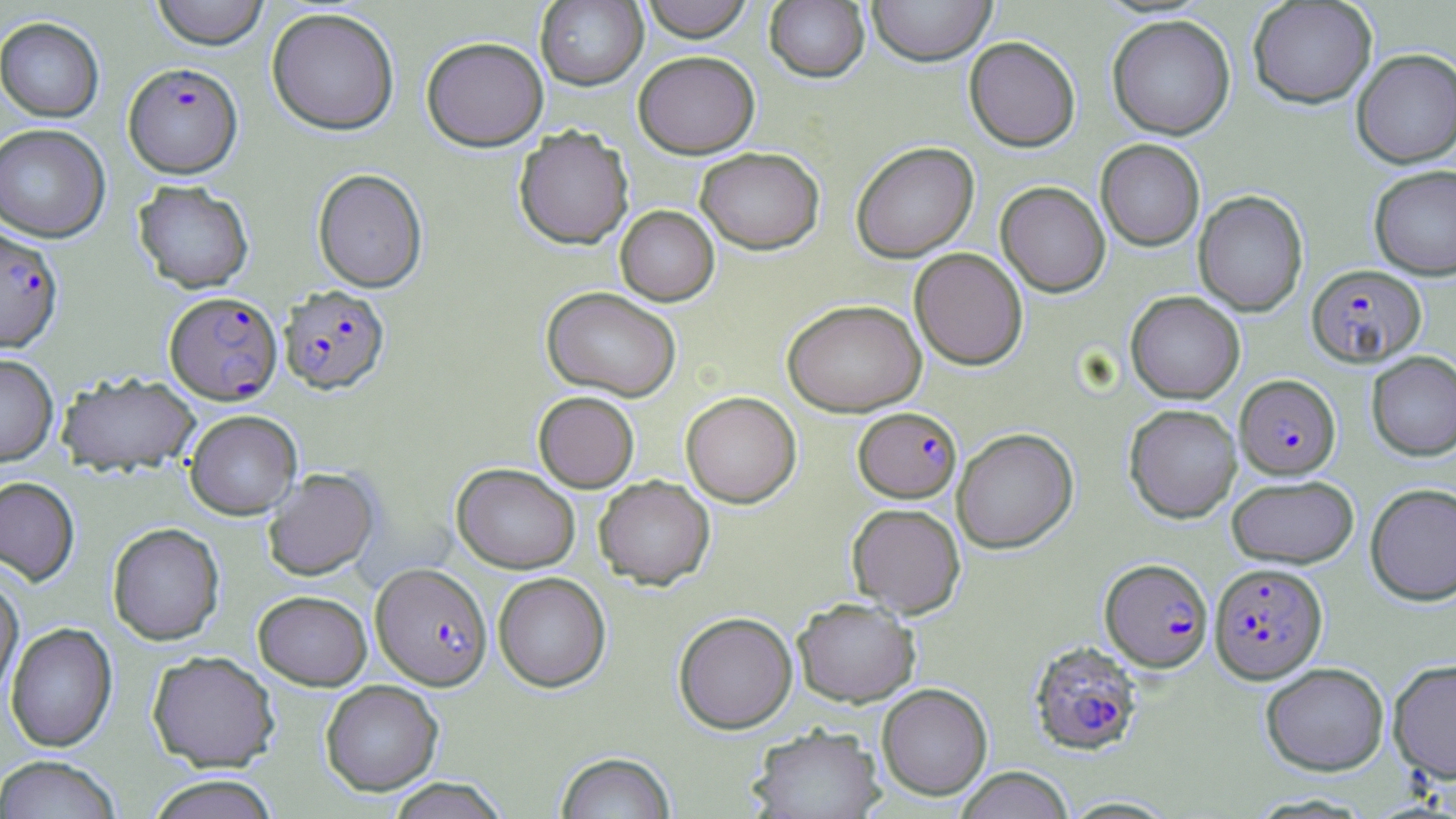

Approximate bounding boxes as (x1, y1, x2, y2) in pixels. Plasmodium falciparum-infected red blood cell locations: (123, 61, 243, 178), (0, 226, 64, 353), (1306, 264, 1426, 368), (279, 285, 390, 394), (165, 291, 282, 404), (1235, 374, 1340, 479), (854, 407, 961, 502), (1100, 558, 1213, 672), (370, 562, 492, 690), (1209, 562, 1328, 683), (1028, 640, 1144, 756). Uninfected red blood cell locations: (150, 0, 270, 49), (639, 0, 754, 41), (867, 0, 997, 66), (535, 1, 648, 90), (764, 1, 870, 83), (1247, 1, 1377, 108), (266, 6, 400, 135), (1107, 14, 1236, 140), (0, 16, 104, 122), (421, 36, 549, 151), (964, 36, 1081, 151), (1351, 48, 1456, 168), (634, 50, 760, 158), (0, 123, 111, 242), (514, 125, 633, 249), (1095, 139, 1205, 251), (851, 141, 979, 262), (695, 147, 824, 254), (1369, 165, 1456, 280), (312, 168, 428, 293), (133, 179, 255, 293), (996, 181, 1110, 296), (1193, 190, 1308, 317), (615, 205, 719, 305), (910, 247, 1028, 370), (541, 286, 682, 401), (1126, 291, 1245, 403), (782, 299, 926, 416), (1367, 351, 1456, 460), (0, 353, 58, 466), (57, 372, 201, 474), (533, 391, 640, 492), (680, 391, 801, 508), (1124, 404, 1242, 523), (185, 410, 302, 520), (952, 427, 1078, 553), (452, 463, 580, 573), (263, 468, 379, 581), (1227, 474, 1358, 568), (593, 475, 715, 590), (0, 476, 80, 586), (1365, 482, 1456, 605), (846, 502, 966, 618), (107, 522, 224, 645), (493, 571, 611, 692), (0, 572, 24, 703), (253, 589, 372, 691), (793, 597, 920, 707), (673, 611, 797, 733), (5, 621, 117, 752), (147, 650, 280, 772), (1388, 658, 1456, 783), (1260, 662, 1390, 776), (320, 680, 443, 795), (877, 683, 993, 800), (748, 723, 885, 819), (556, 752, 676, 819), (0, 755, 123, 819), (954, 766, 1074, 819), (145, 774, 280, 819), (385, 777, 510, 818). Slide-level diagnosis: Plasmodium falciparum. May-Grünwald-Giemsa stain. Thin blood smear. Light microscopy. Single field of view. Captured at 1000x magnification. Image is 1456×819 pixels.